Outline platelets.
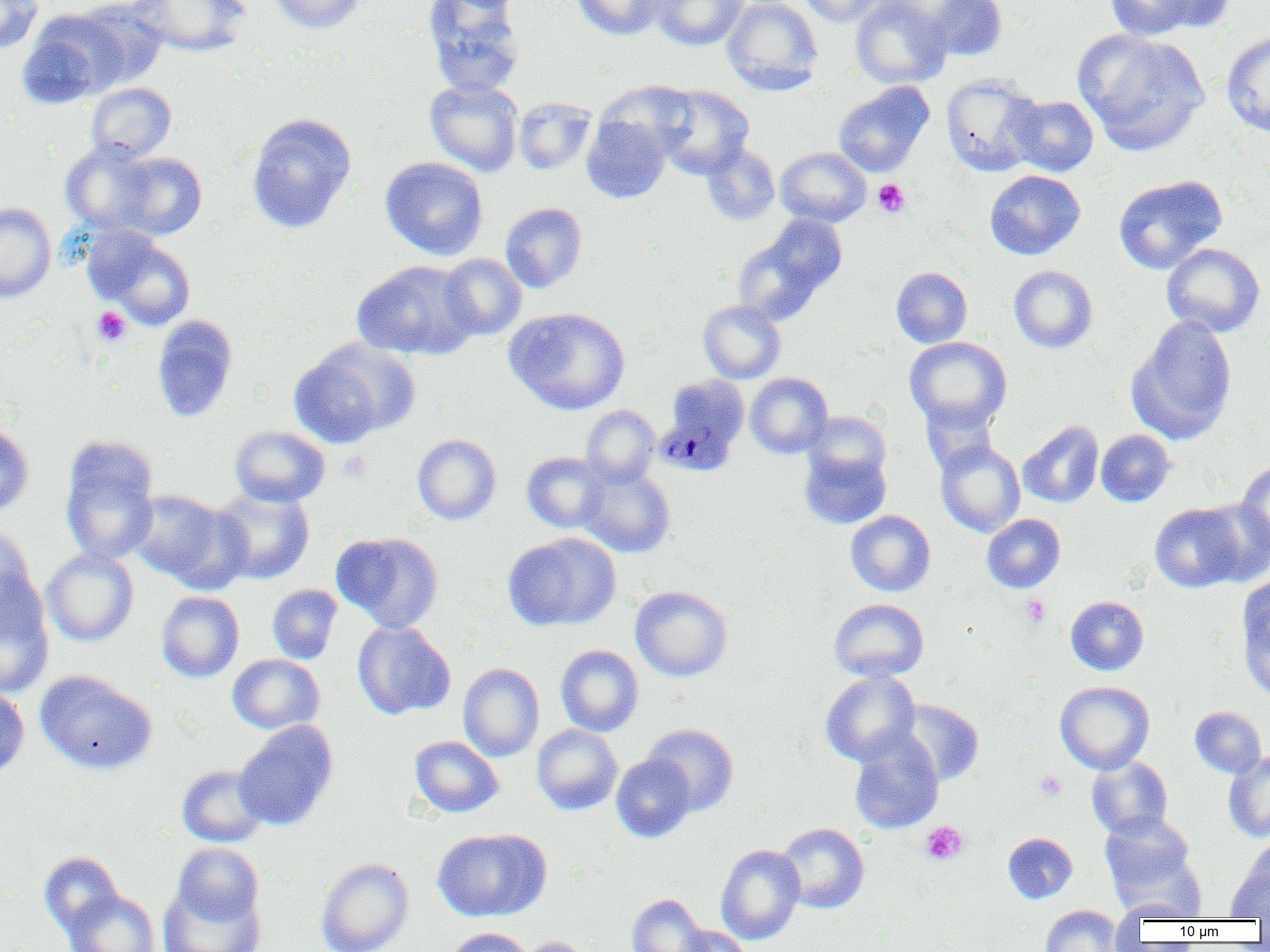
Approximate bounding boxes as named x1/y1/x2/y2 corners in pixels.
Platelets: (x1=873, y1=179, x2=910, y2=217), (x1=91, y1=306, x2=131, y2=347), (x1=339, y1=451, x2=372, y2=482), (x1=1021, y1=595, x2=1050, y2=628), (x1=1035, y1=770, x2=1066, y2=802), (x1=920, y1=821, x2=968, y2=864).

slide-level diagnosis = Plasmodium malariae
field of view = single
uninfected red blood cell locations = approximate bounding boxes as named x1/y1/x2/y2 corners in pixels: (x1=0, y1=0, x2=43, y2=53), (x1=131, y1=0, x2=251, y2=56), (x1=266, y1=0, x2=367, y2=34), (x1=422, y1=0, x2=526, y2=97), (x1=571, y1=0, x2=665, y2=40), (x1=649, y1=0, x2=748, y2=50), (x1=722, y1=0, x2=823, y2=95), (x1=799, y1=0, x2=886, y2=26), (x1=850, y1=0, x2=951, y2=89), (x1=922, y1=0, x2=1007, y2=61), (x1=1101, y1=0, x2=1211, y2=39), (x1=1148, y1=0, x2=1236, y2=33), (x1=72, y1=1, x2=170, y2=88), (x1=17, y1=12, x2=126, y2=108), (x1=1073, y1=29, x2=1208, y2=156), (x1=1222, y1=32, x2=1270, y2=137), (x1=940, y1=73, x2=1044, y2=176), (x1=425, y1=79, x2=523, y2=176), (x1=597, y1=80, x2=696, y2=159), (x1=86, y1=82, x2=176, y2=163), (x1=833, y1=82, x2=934, y2=177), (x1=655, y1=85, x2=754, y2=179), (x1=1010, y1=96, x2=1098, y2=177), (x1=513, y1=97, x2=596, y2=175), (x1=247, y1=113, x2=357, y2=233), (x1=581, y1=115, x2=671, y2=203), (x1=61, y1=141, x2=158, y2=235), (x1=701, y1=143, x2=780, y2=226), (x1=775, y1=147, x2=871, y2=227), (x1=114, y1=152, x2=206, y2=240), (x1=380, y1=157, x2=488, y2=260), (x1=984, y1=170, x2=1085, y2=260), (x1=1113, y1=175, x2=1227, y2=274), (x1=0, y1=202, x2=56, y2=303), (x1=500, y1=202, x2=587, y2=293), (x1=733, y1=216, x2=846, y2=325), (x1=93, y1=230, x2=197, y2=330), (x1=1162, y1=243, x2=1265, y2=338), (x1=439, y1=254, x2=527, y2=340), (x1=352, y1=260, x2=478, y2=360), (x1=1009, y1=265, x2=1097, y2=353), (x1=891, y1=267, x2=972, y2=348), (x1=698, y1=300, x2=785, y2=384), (x1=504, y1=307, x2=630, y2=414), (x1=151, y1=315, x2=238, y2=422), (x1=1128, y1=316, x2=1237, y2=444), (x1=904, y1=337, x2=1012, y2=431), (x1=289, y1=340, x2=416, y2=447), (x1=745, y1=372, x2=833, y2=458), (x1=668, y1=376, x2=749, y2=447), (x1=920, y1=401, x2=999, y2=475), (x1=581, y1=405, x2=660, y2=487), (x1=803, y1=411, x2=891, y2=484), (x1=0, y1=421, x2=34, y2=518), (x1=1018, y1=421, x2=1104, y2=508), (x1=229, y1=425, x2=330, y2=507), (x1=1096, y1=430, x2=1175, y2=507), (x1=412, y1=434, x2=501, y2=525), (x1=60, y1=440, x2=160, y2=566), (x1=935, y1=440, x2=1025, y2=537), (x1=799, y1=448, x2=891, y2=529), (x1=522, y1=452, x2=609, y2=533), (x1=1235, y1=460, x2=1270, y2=556), (x1=577, y1=466, x2=675, y2=557), (x1=212, y1=487, x2=315, y2=584), (x1=128, y1=490, x2=225, y2=583), (x1=162, y1=500, x2=253, y2=594), (x1=1149, y1=502, x2=1245, y2=592), (x1=1190, y1=502, x2=1270, y2=587), (x1=846, y1=510, x2=935, y2=597), (x1=982, y1=514, x2=1066, y2=593), (x1=0, y1=524, x2=37, y2=620), (x1=332, y1=531, x2=444, y2=633), (x1=503, y1=532, x2=621, y2=630), (x1=42, y1=547, x2=139, y2=647), (x1=0, y1=574, x2=54, y2=699), (x1=1239, y1=583, x2=1269, y2=700), (x1=267, y1=584, x2=342, y2=664), (x1=630, y1=585, x2=732, y2=681), (x1=157, y1=591, x2=244, y2=682), (x1=1066, y1=596, x2=1149, y2=675), (x1=829, y1=598, x2=929, y2=682), (x1=352, y1=621, x2=456, y2=720), (x1=555, y1=644, x2=643, y2=737), (x1=227, y1=654, x2=325, y2=733), (x1=458, y1=663, x2=544, y2=761), (x1=35, y1=670, x2=157, y2=774), (x1=820, y1=670, x2=920, y2=766), (x1=1055, y1=681, x2=1154, y2=774), (x1=0, y1=686, x2=30, y2=781), (x1=895, y1=699, x2=984, y2=787), (x1=1189, y1=706, x2=1266, y2=778), (x1=234, y1=720, x2=338, y2=830), (x1=642, y1=723, x2=739, y2=816), (x1=532, y1=724, x2=622, y2=815), (x1=849, y1=731, x2=944, y2=834), (x1=409, y1=736, x2=503, y2=817), (x1=1223, y1=751, x2=1270, y2=842), (x1=611, y1=753, x2=697, y2=843), (x1=1086, y1=756, x2=1173, y2=838), (x1=177, y1=765, x2=269, y2=847), (x1=1099, y1=812, x2=1195, y2=894), (x1=776, y1=823, x2=869, y2=914), (x1=432, y1=828, x2=551, y2=921), (x1=1002, y1=832, x2=1077, y2=903), (x1=173, y1=842, x2=264, y2=925), (x1=1111, y1=842, x2=1205, y2=919), (x1=716, y1=844, x2=805, y2=945), (x1=39, y1=851, x2=124, y2=937), (x1=1227, y1=852, x2=1270, y2=919), (x1=316, y1=857, x2=414, y2=952), (x1=158, y1=885, x2=266, y2=952), (x1=64, y1=890, x2=161, y2=952), (x1=627, y1=893, x2=710, y2=952), (x1=1113, y1=900, x2=1200, y2=924), (x1=1039, y1=904, x2=1123, y2=952), (x1=674, y1=925, x2=752, y2=952), (x1=445, y1=927, x2=534, y2=952), (x1=515, y1=936, x2=594, y2=952)
image size = 1270×952 pixels
Plasmodium malariae-infected red blood cell locations = approximate bounding boxes as named x1/y1/x2/y2 corners in pixels: (x1=655, y1=416, x2=737, y2=475)
magnification = 1000x
modality = light microscopy
preparation = thin blood smear